Outline each Plasmodium malariae-infected red blood cell.
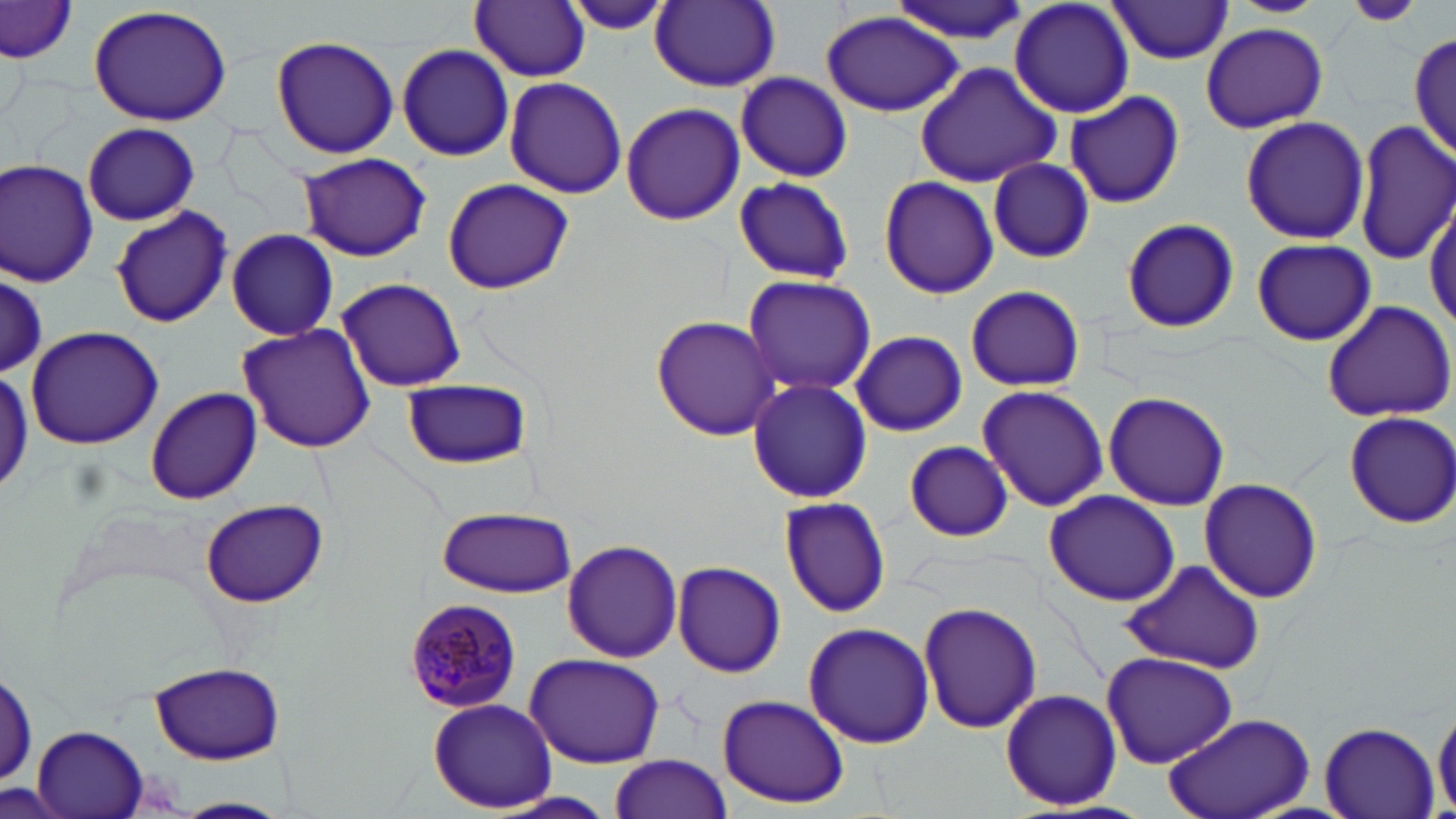
Approximate bounding boxes as (x1,y1)-(x2,y2) corner pairs in pixels.
Plasmodium malariae-infected red blood cells: (402,597)-(523,712).

Uninfected red blood cell locations (subset): (558,0)-(682,35), (890,0)-(1030,45), (1010,0)-(1135,118), (1227,0)-(1328,18), (1340,0)-(1426,25), (471,1)-(590,82), (651,1)-(780,91), (1105,2)-(1235,64), (0,3)-(78,65), (86,5)-(233,128), (821,12)-(964,117), (1201,22)-(1327,132), (1411,27)-(1456,162), (270,35)-(401,158), (396,44)-(515,161), (916,60)-(1064,188), (735,71)-(852,182), (504,76)-(627,199), (1063,91)-(1185,209), (621,101)-(743,228), (1238,115)-(1370,246), (1353,119)-(1456,266), (82,123)-(199,226), (296,152)-(433,263), (1,158)-(99,287), (987,158)-(1094,263), (878,174)-(998,301), (732,175)-(854,285), (442,178)-(576,293), (1426,194)-(1456,331), (111,206)-(231,328), (1119,216)-(1241,334), (225,228)-(338,341), (1251,237)-(1376,346), (2,275)-(46,375), (740,275)-(877,394), (334,276)-(467,391), (963,284)-(1086,393), (1321,300)-(1456,423), (651,315)-(780,442), (236,323)-(376,453), (24,325)-(164,451), (851,331)-(967,437), (400,376)-(533,470), (745,378)-(874,503), (978,384)-(1108,511), (145,388)-(261,504), (1102,390)-(1231,510), (1343,412)-(1456,528), (905,441)-(1015,541), (1199,477)-(1324,605), (1043,489)-(1180,606), (777,497)-(894,615), (197,498)-(331,605), (436,505)-(576,597), (560,539)-(684,663), (1120,559)-(1264,675), (672,561)-(786,677), (917,602)-(1042,734), (803,622)-(936,750), (524,649)-(665,767), (1102,652)-(1240,768), (150,661)-(287,765), (0,664)-(37,793), (1001,687)-(1122,809), (717,693)-(850,809), (428,698)-(557,812), (1433,701)-(1456,815), (1161,713)-(1316,819), (1318,723)-(1439,818), (607,752)-(734,819), (493,794)-(619,819), (173,796)-(290,817). Slide-level diagnosis: Plasmodium malariae. Single field of view. 1000x magnification. Thin blood film. Optical microscopy. Image is 1456×819 pixels. May-Grünwald-Giemsa stain.